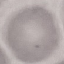

Result: negative for malaria parasites. Thin smear of blood. Photographed with a smartphone camera at the microscope eyepiece. Cell patch, automatically extracted from a larger field of view and resized to 64 × 64 pixels. Giemsa stain.